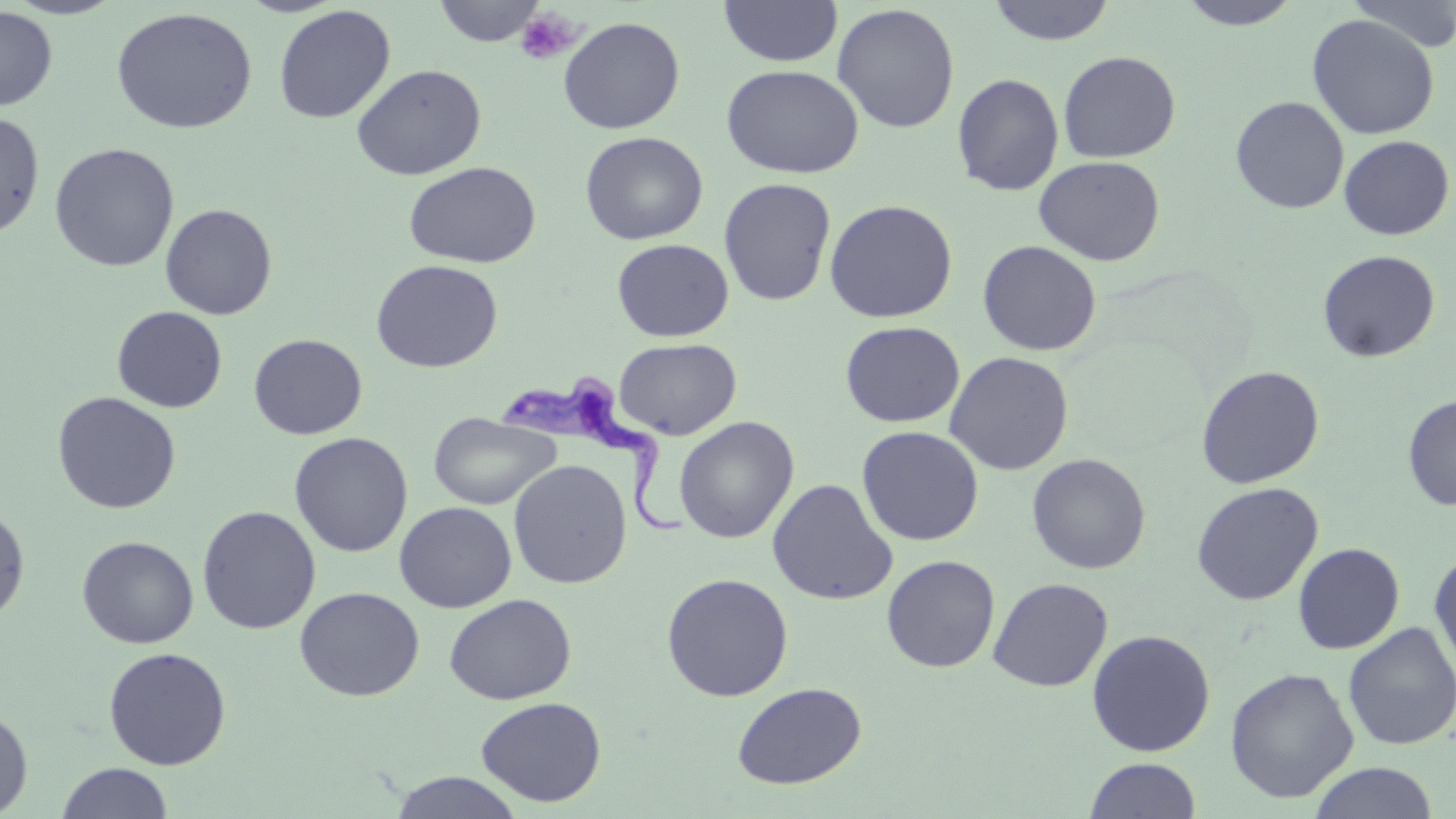

Approximate bounding boxes as (x1,y1)-(x2,y2) corner pairs in pixels. Trypanosoma brucei locations: (501,373)-(689,540). Uninfected red blood cell locations: (4,0)-(125,20), (432,0)-(547,46), (718,0)-(843,67), (986,0)-(1116,45), (1176,0)-(1302,31), (1344,0)-(1456,53), (831,3)-(960,133), (273,4)-(395,124), (0,7)-(58,111), (111,7)-(258,135), (1306,14)-(1440,140), (558,16)-(685,134), (1058,50)-(1181,163), (351,63)-(487,180), (721,64)-(864,178), (951,72)-(1065,196), (1230,96)-(1350,214), (0,111)-(45,238), (579,131)-(708,245), (1339,135)-(1454,240), (49,142)-(179,272), (1033,155)-(1165,266), (403,161)-(541,268), (718,177)-(837,307), (823,199)-(958,323), (160,203)-(278,320), (612,238)-(733,342), (977,240)-(1102,356), (1317,249)-(1441,362), (370,259)-(503,373), (112,307)-(227,413), (840,321)-(965,427), (248,333)-(367,440), (613,338)-(741,439), (944,351)-(1074,475), (1195,365)-(1325,489), (52,391)-(181,514), (1402,393)-(1456,511), (428,411)-(560,511), (674,416)-(799,543), (856,426)-(984,546), (289,432)-(413,558), (1026,453)-(1151,574), (508,459)-(632,589), (767,478)-(898,605), (1190,481)-(1323,606), (394,501)-(516,612), (0,504)-(31,626), (197,505)-(321,635), (77,535)-(198,648), (1292,542)-(1405,654), (1429,550)-(1456,677), (882,554)-(1000,672), (660,572)-(794,702), (988,577)-(1113,692), (293,586)-(425,701), (444,594)-(576,705), (1342,622)-(1455,751), (1086,629)-(1216,756), (103,646)-(231,770), (1225,667)-(1359,803), (732,682)-(866,789), (475,696)-(607,807), (0,707)-(33,817), (1083,758)-(1202,818), (1308,762)-(1439,819), (55,763)-(174,819), (388,771)-(525,818). Platelet locations: (516,8)-(579,65). Slide-level diagnosis: Trypanosoma brucei. 1000x magnification. May-Grünwald-Giemsa stain. Thin blood smear. Single field of view. Optical microscopy. Image is 1456×819 pixels.